Comment on the morphology of the red blood cells.
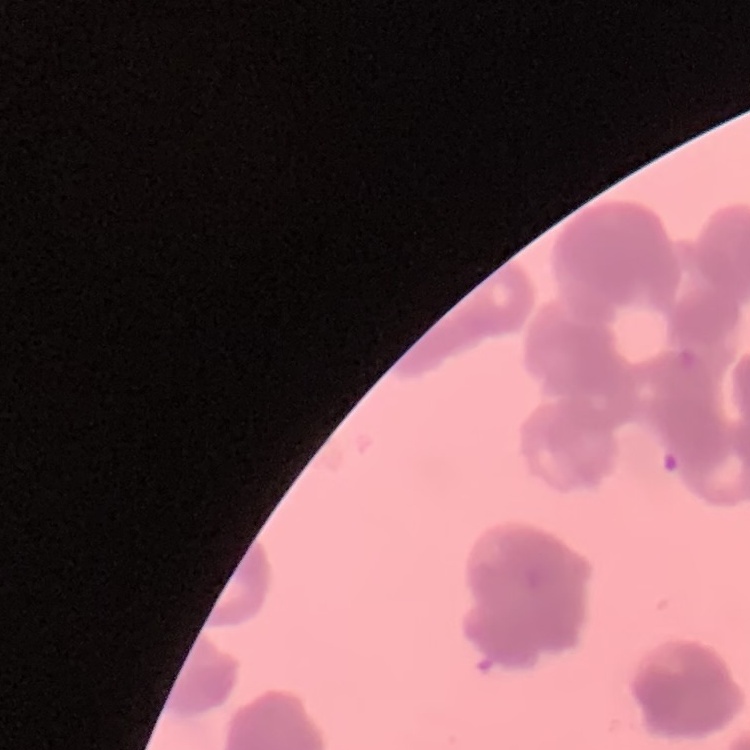

They show rouleaux formation.

Thin blood film. One tile cut from a larger photomicrograph. Stained with either Field's or Giemsa.